Classify this cell by malaria status.
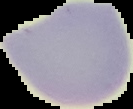
It is uninfected.

Segmented cell region on a black background. Image is 133×109 pixels. From a thin blood smear.